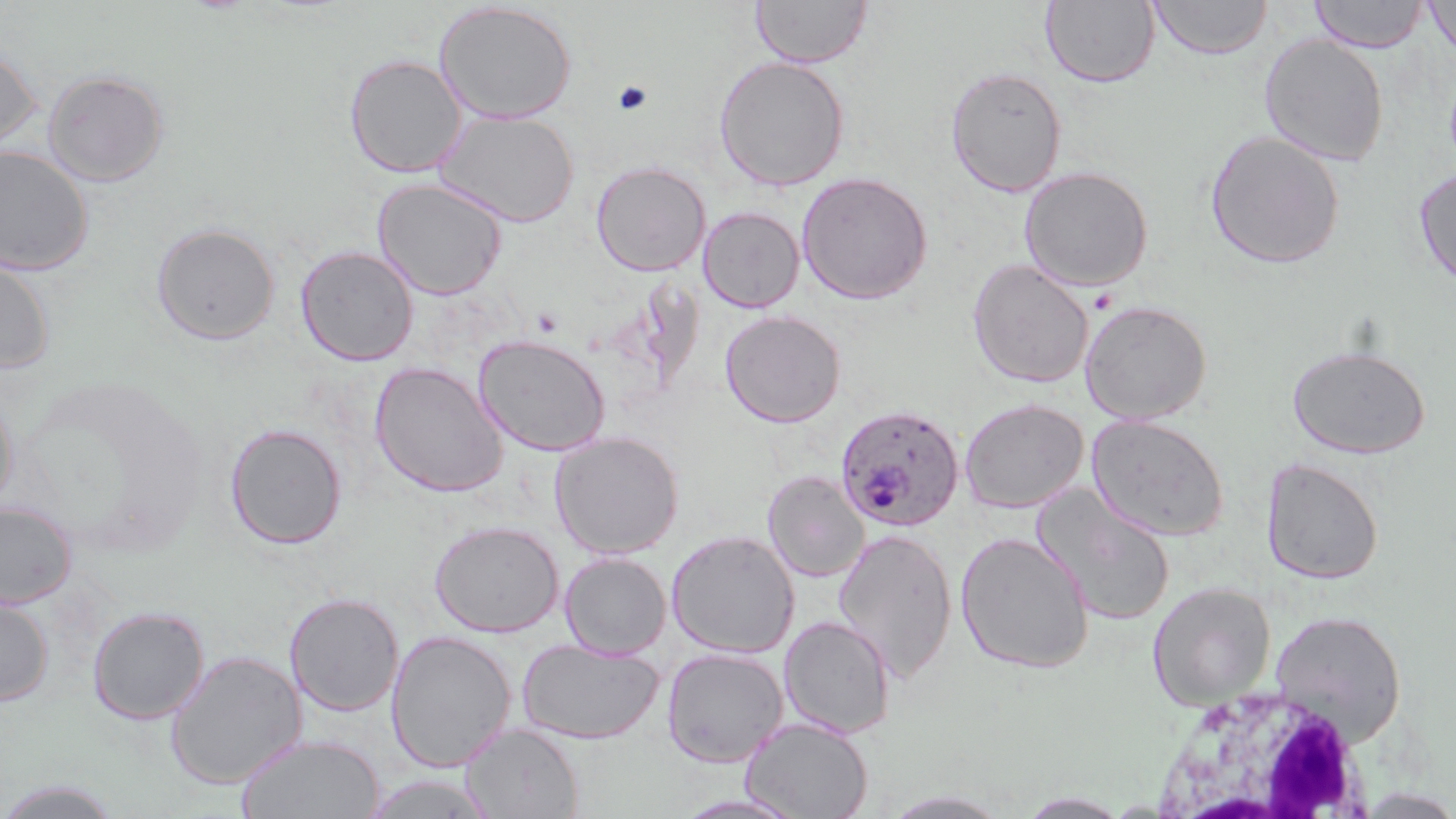
Summary:
  - Coordinate format: approximate bounding boxes as (x1,y1)-(x2,y2) corner pairs in pixels
  - White blood cell locations: (1149,683)-(1372,819)
  - Plasmodium ovale-infected red blood cell locations: (835,403)-(965,531)
  - Platelet locations: (613,80)-(654,115)
  - Uninfected red blood cell locations: (751,0)-(872,68), (1149,0)-(1273,60), (1309,0)-(1429,53), (1423,0)-(1455,61), (1041,1)-(1160,88), (434,2)-(577,124), (1258,32)-(1390,167), (0,42)-(41,159), (344,53)-(468,178), (713,55)-(850,191), (945,65)-(1067,197), (42,70)-(169,186), (434,108)-(578,227), (1204,129)-(1346,269), (0,146)-(94,275), (591,161)-(711,276), (1414,165)-(1456,295), (1019,166)-(1154,291), (797,172)-(933,305), (372,178)-(508,300), (698,206)-(805,312), (150,222)-(281,345), (296,245)-(419,366), (0,253)-(56,375), (967,259)-(1094,388), (1079,299)-(1212,424), (720,309)-(847,428), (473,333)-(611,456), (1287,345)-(1431,459), (370,362)-(508,497), (0,388)-(18,512), (959,398)-(1088,514), (1087,413)-(1229,541), (224,423)-(347,549), (550,431)-(685,559), (1261,458)-(1384,584), (763,470)-(869,582), (1031,484)-(1176,626), (0,501)-(77,609), (429,520)-(563,637), (833,528)-(957,682), (666,530)-(801,658), (955,531)-(1095,673), (560,551)-(672,660), (1148,582)-(1276,708), (0,588)-(54,707), (284,592)-(404,716), (87,606)-(210,724), (1270,610)-(1407,744), (779,616)-(896,738), (385,630)-(516,773), (516,637)-(664,745), (662,647)-(788,767), (164,650)-(307,791), (740,716)-(873,818), (460,722)-(586,819), (235,734)-(385,818), (358,773)-(499,818), (0,778)-(125,818), (672,792)-(808,818)
  - Slide-level diagnosis: Plasmodium ovale
  - Magnification: 1000x
  - Stain: May-Grünwald-Giemsa
  - Field of view: one of a larger specimen
  - Preparation: thin blood film
  - Modality: optical microscopy
  - Image size: 1456×819 pixels